Report the malaria status of this cell.
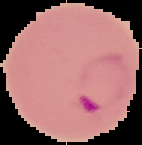

Parasitized.

Summary:
  - Image type: segmented cell region with the area outside set to black
  - Image size: 142×145 pixels
  - Preparation: thin blood smear